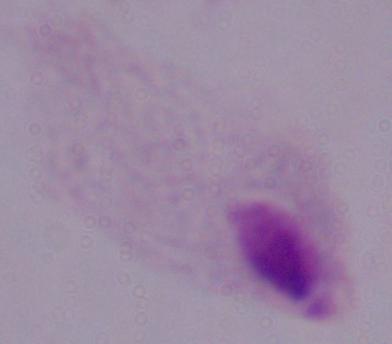
{
  "identification": "trichomonad",
  "modality": "micrograph",
  "magnification": "1000x"
}